Assess this cell for malaria.
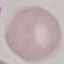
It is uninfected.

Giemsa stain. Cell patch, automatically extracted from a larger field of view and resized to 64 × 64 pixels. Acquired by smartphone through the microscope eyepiece. Thin blood smear.